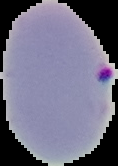

image size = 118×166 pixels
malaria status = parasitized
image type = segmented cell region with the area outside set to black
preparation = thin blood smear